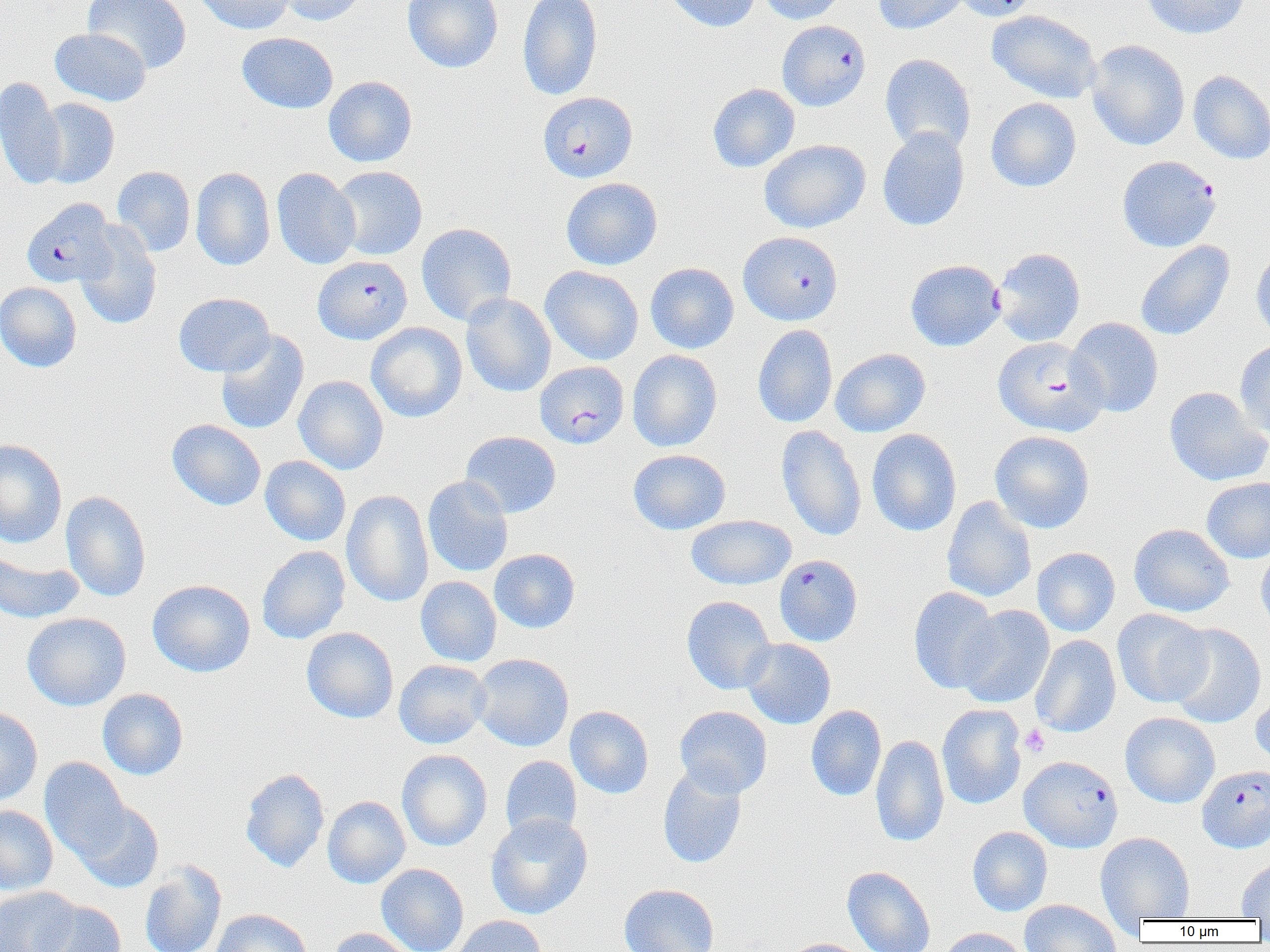

Summary:
  - Coordinate format: approximate bounding boxes as named x1/y1/x2/y2 corners in pixels
  - Platelet locations: (x1=1020, y1=724, x2=1050, y2=757)
  - Plasmodium falciparum-infected red blood cell locations (subset): (x1=537, y1=90, x2=638, y2=182), (x1=1117, y1=156, x2=1221, y2=252), (x1=21, y1=198, x2=118, y2=288), (x1=738, y1=231, x2=843, y2=325), (x1=992, y1=248, x2=1086, y2=346), (x1=312, y1=255, x2=412, y2=345), (x1=993, y1=336, x2=1107, y2=436), (x1=774, y1=554, x2=863, y2=646), (x1=1019, y1=755, x2=1123, y2=853), (x1=1197, y1=765, x2=1270, y2=853)
  - Uninfected red blood cell locations (subset): (x1=83, y1=0, x2=192, y2=74), (x1=193, y1=0, x2=296, y2=34), (x1=275, y1=0, x2=370, y2=26), (x1=403, y1=0, x2=503, y2=73), (x1=517, y1=0, x2=603, y2=101), (x1=663, y1=0, x2=761, y2=33), (x1=755, y1=0, x2=847, y2=24), (x1=873, y1=0, x2=968, y2=35), (x1=950, y1=0, x2=1041, y2=21), (x1=1141, y1=0, x2=1251, y2=39), (x1=987, y1=9, x2=1103, y2=104), (x1=50, y1=27, x2=151, y2=106), (x1=237, y1=32, x2=338, y2=113), (x1=1086, y1=40, x2=1190, y2=151), (x1=880, y1=54, x2=976, y2=154), (x1=1188, y1=70, x2=1270, y2=164), (x1=323, y1=76, x2=417, y2=167), (x1=0, y1=77, x2=67, y2=190), (x1=708, y1=84, x2=800, y2=172), (x1=36, y1=98, x2=120, y2=188), (x1=986, y1=98, x2=1081, y2=192), (x1=877, y1=127, x2=970, y2=232), (x1=759, y1=139, x2=871, y2=233), (x1=111, y1=166, x2=196, y2=256), (x1=331, y1=166, x2=427, y2=260), (x1=190, y1=167, x2=276, y2=271), (x1=272, y1=167, x2=360, y2=270), (x1=561, y1=177, x2=662, y2=270), (x1=416, y1=222, x2=517, y2=326), (x1=75, y1=224, x2=163, y2=330), (x1=1135, y1=240, x2=1235, y2=341), (x1=1251, y1=246, x2=1270, y2=342), (x1=905, y1=259, x2=1005, y2=351), (x1=645, y1=262, x2=739, y2=354), (x1=540, y1=266, x2=644, y2=365), (x1=0, y1=281, x2=82, y2=373), (x1=461, y1=292, x2=556, y2=397), (x1=173, y1=293, x2=275, y2=377), (x1=1066, y1=317, x2=1163, y2=417), (x1=366, y1=322, x2=467, y2=422), (x1=752, y1=324, x2=838, y2=428), (x1=215, y1=330, x2=309, y2=434), (x1=1234, y1=341, x2=1270, y2=441), (x1=830, y1=348, x2=931, y2=437), (x1=627, y1=349, x2=722, y2=451), (x1=293, y1=375, x2=389, y2=474), (x1=1164, y1=386, x2=1270, y2=487), (x1=167, y1=419, x2=266, y2=511), (x1=776, y1=424, x2=866, y2=541), (x1=866, y1=428, x2=962, y2=536), (x1=990, y1=430, x2=1095, y2=533), (x1=460, y1=431, x2=561, y2=518), (x1=0, y1=439, x2=67, y2=548), (x1=628, y1=449, x2=731, y2=535), (x1=260, y1=456, x2=351, y2=546), (x1=423, y1=476, x2=513, y2=577), (x1=1201, y1=477, x2=1270, y2=563), (x1=60, y1=490, x2=151, y2=602), (x1=341, y1=490, x2=434, y2=607), (x1=941, y1=497, x2=1036, y2=602), (x1=686, y1=515, x2=796, y2=590), (x1=1129, y1=524, x2=1234, y2=617), (x1=1256, y1=544, x2=1270, y2=635), (x1=257, y1=545, x2=351, y2=644), (x1=1032, y1=547, x2=1120, y2=637), (x1=0, y1=548, x2=84, y2=625), (x1=489, y1=549, x2=580, y2=633), (x1=416, y1=576, x2=501, y2=666), (x1=147, y1=579, x2=255, y2=677), (x1=908, y1=587, x2=1002, y2=694), (x1=681, y1=596, x2=777, y2=694), (x1=955, y1=605, x2=1055, y2=708), (x1=1112, y1=608, x2=1212, y2=707), (x1=22, y1=613, x2=131, y2=711), (x1=1167, y1=623, x2=1266, y2=728), (x1=301, y1=627, x2=398, y2=723), (x1=1030, y1=635, x2=1121, y2=738), (x1=741, y1=638, x2=836, y2=729), (x1=471, y1=653, x2=574, y2=751), (x1=394, y1=659, x2=491, y2=749), (x1=97, y1=688, x2=188, y2=780), (x1=1250, y1=692, x2=1270, y2=772), (x1=937, y1=704, x2=1027, y2=809), (x1=806, y1=705, x2=887, y2=801), (x1=565, y1=706, x2=654, y2=799), (x1=674, y1=706, x2=772, y2=797), (x1=0, y1=707, x2=43, y2=807), (x1=1120, y1=712, x2=1220, y2=808), (x1=871, y1=735, x2=949, y2=848), (x1=396, y1=749, x2=492, y2=851), (x1=39, y1=756, x2=132, y2=862), (x1=500, y1=756, x2=582, y2=841), (x1=657, y1=763, x2=747, y2=868), (x1=240, y1=768, x2=329, y2=873), (x1=322, y1=796, x2=411, y2=889), (x1=73, y1=800, x2=163, y2=893), (x1=0, y1=805, x2=58, y2=894), (x1=485, y1=814, x2=593, y2=919), (x1=967, y1=826, x2=1052, y2=916), (x1=1096, y1=833, x2=1195, y2=921), (x1=1236, y1=857, x2=1270, y2=919), (x1=139, y1=860, x2=227, y2=952), (x1=376, y1=863, x2=468, y2=952), (x1=842, y1=866, x2=936, y2=952), (x1=619, y1=883, x2=720, y2=952), (x1=0, y1=886, x2=81, y2=952), (x1=34, y1=898, x2=126, y2=952), (x1=1020, y1=899, x2=1122, y2=952), (x1=210, y1=908, x2=312, y2=952), (x1=451, y1=915, x2=547, y2=952), (x1=939, y1=927, x2=1031, y2=952), (x1=328, y1=928, x2=416, y2=952), (x1=784, y1=938, x2=873, y2=952)
  - Slide-level diagnosis: Plasmodium falciparum
  - Magnification: 1000x
  - Preparation: thin blood smear
  - Field of view: single
  - Image size: 1270×952 pixels
  - Modality: light microscopy